Report the malaria status of this cell.
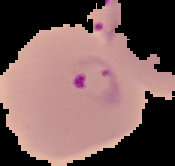

It is parasitized.

image_type: segmented cell region with the area outside set to black
preparation: thin blood smear
image_size: 175×166 pixels